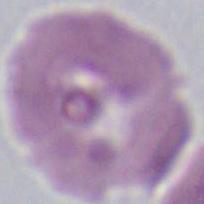
An erythrocyte is seen. Micrograph. Captured at 1000x magnification.